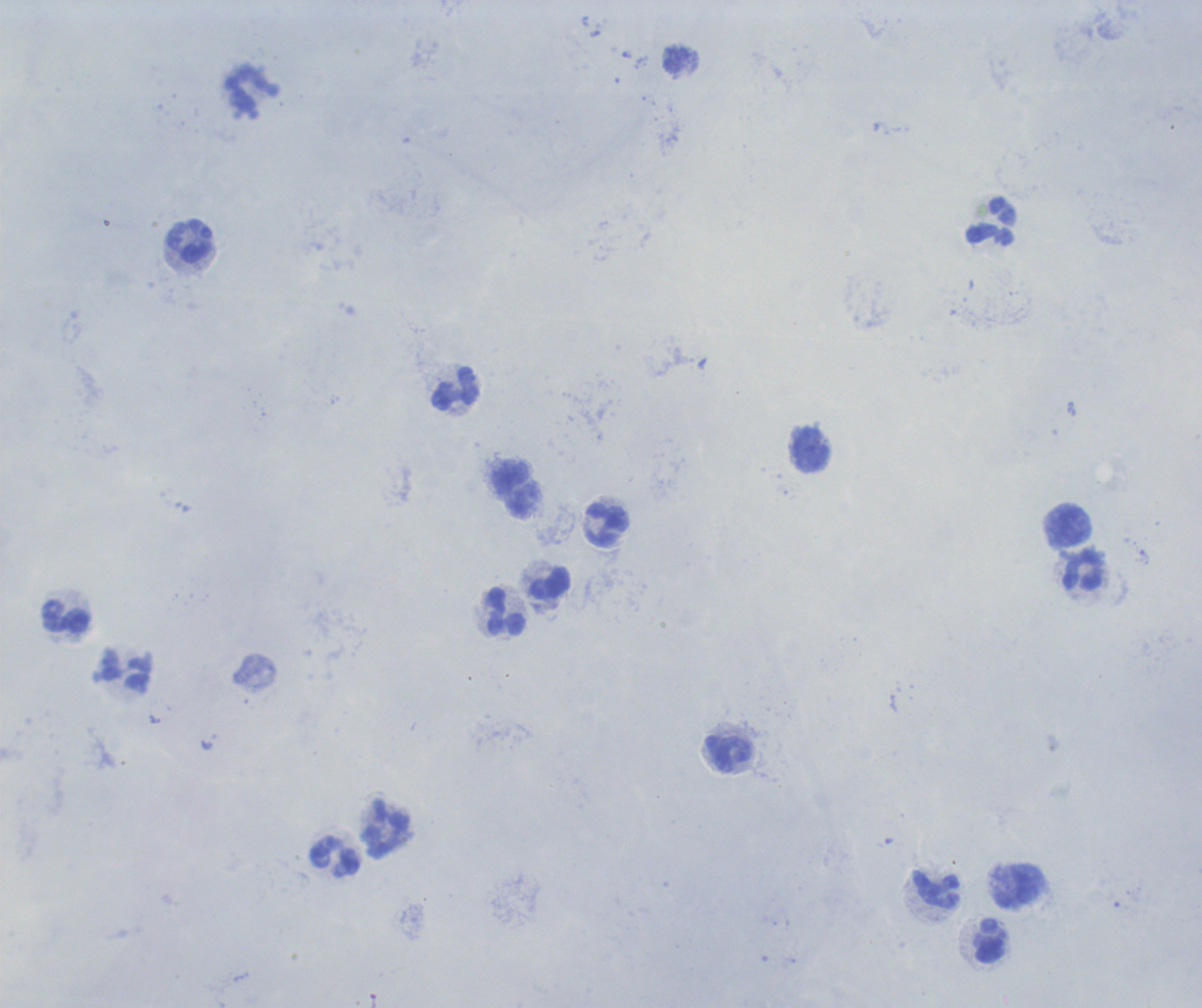 Approximate centers as (x, y) in pixels. Leukocyte locations: (254, 94), (993, 222), (191, 242), (457, 389), (812, 449), (607, 525), (1069, 527), (1084, 572), (550, 583), (506, 611), (67, 617), (730, 755), (385, 829), (336, 858), (1020, 888), (936, 889), (991, 942). Single field of view. 100x magnification. Result: no malaria parasites detected. Romanowsky stain. Image is 1202×1008 pixels. Previously used in an actual diagnosis. Thick smear of blood. Background quality: poor.